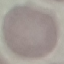
malaria status = uninfected
capture = smartphone through the microscope eyepiece
image type = automatically extracted cell patch, resized to 64 × 64 pixels
preparation = thin blood film
stain = Giemsa